Outline each blood parasite and name the species.
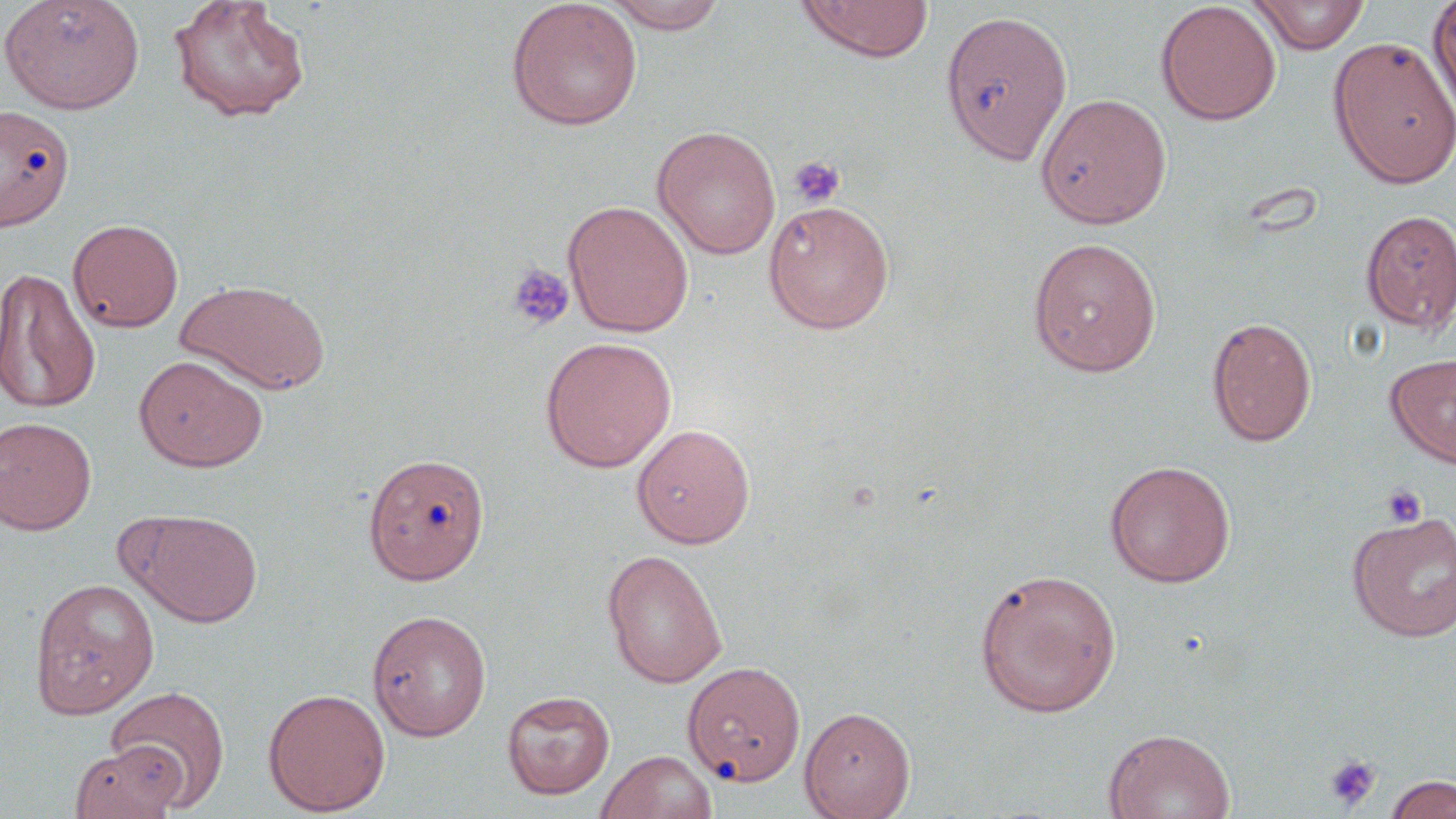

No blood parasites observed.

Summary:
  - Coordinate format: approximate bounding boxes as (x1, y1, x2, y2) in pixels
  - Platelet locations: (787, 155, 846, 208), (506, 263, 575, 331), (1381, 484, 1427, 527), (1323, 753, 1382, 811)
  - Uninfected red blood cell locations: (0, 0, 146, 115), (168, 0, 311, 123), (505, 0, 643, 131), (600, 0, 731, 33), (1426, 0, 1456, 125), (796, 1, 935, 62), (1154, 1, 1282, 126), (1248, 1, 1371, 54), (939, 9, 1073, 165), (1328, 36, 1455, 189), (1035, 92, 1172, 229), (0, 104, 75, 230), (652, 125, 781, 259), (563, 200, 694, 337), (763, 200, 895, 334), (1359, 209, 1456, 334), (67, 218, 184, 333), (1026, 236, 1162, 376), (0, 267, 101, 415), (176, 278, 332, 395), (1206, 316, 1317, 447), (539, 336, 677, 473), (1385, 352, 1456, 469), (133, 354, 268, 472), (0, 415, 97, 535), (631, 423, 756, 548), (363, 452, 490, 584), (1104, 460, 1236, 587), (128, 509, 264, 627), (1347, 510, 1456, 642), (602, 548, 728, 688), (973, 567, 1123, 718), (29, 577, 159, 718), (367, 609, 492, 741), (683, 660, 806, 788), (105, 685, 230, 810), (263, 687, 391, 815), (501, 690, 616, 799), (799, 705, 916, 819), (1103, 727, 1235, 819), (70, 742, 185, 819), (596, 749, 718, 819), (1384, 774, 1456, 819)
  - Slide-level diagnosis: no evidence of blood parasites
  - Stain: May-Grünwald-Giemsa
  - Image size: 1456×819 pixels
  - Preparation: thin blood film
  - Modality: light microscopy
  - Magnification: 1000x
  - Field of view: one of a larger specimen